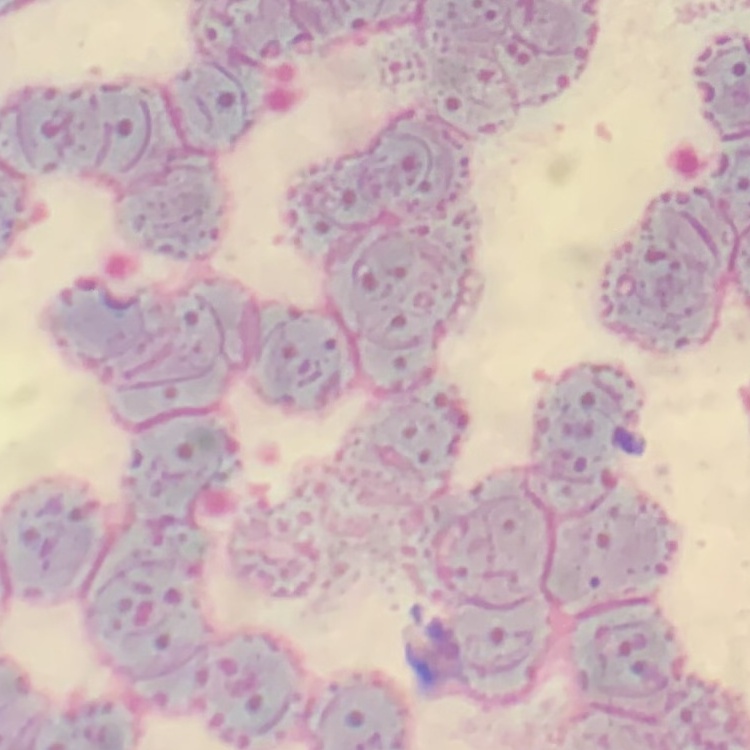 The red blood cells exhibit rouleaux formation. One tile cut from a larger photomicrograph. Stained with either Field's or Giemsa. Thin blood smear.